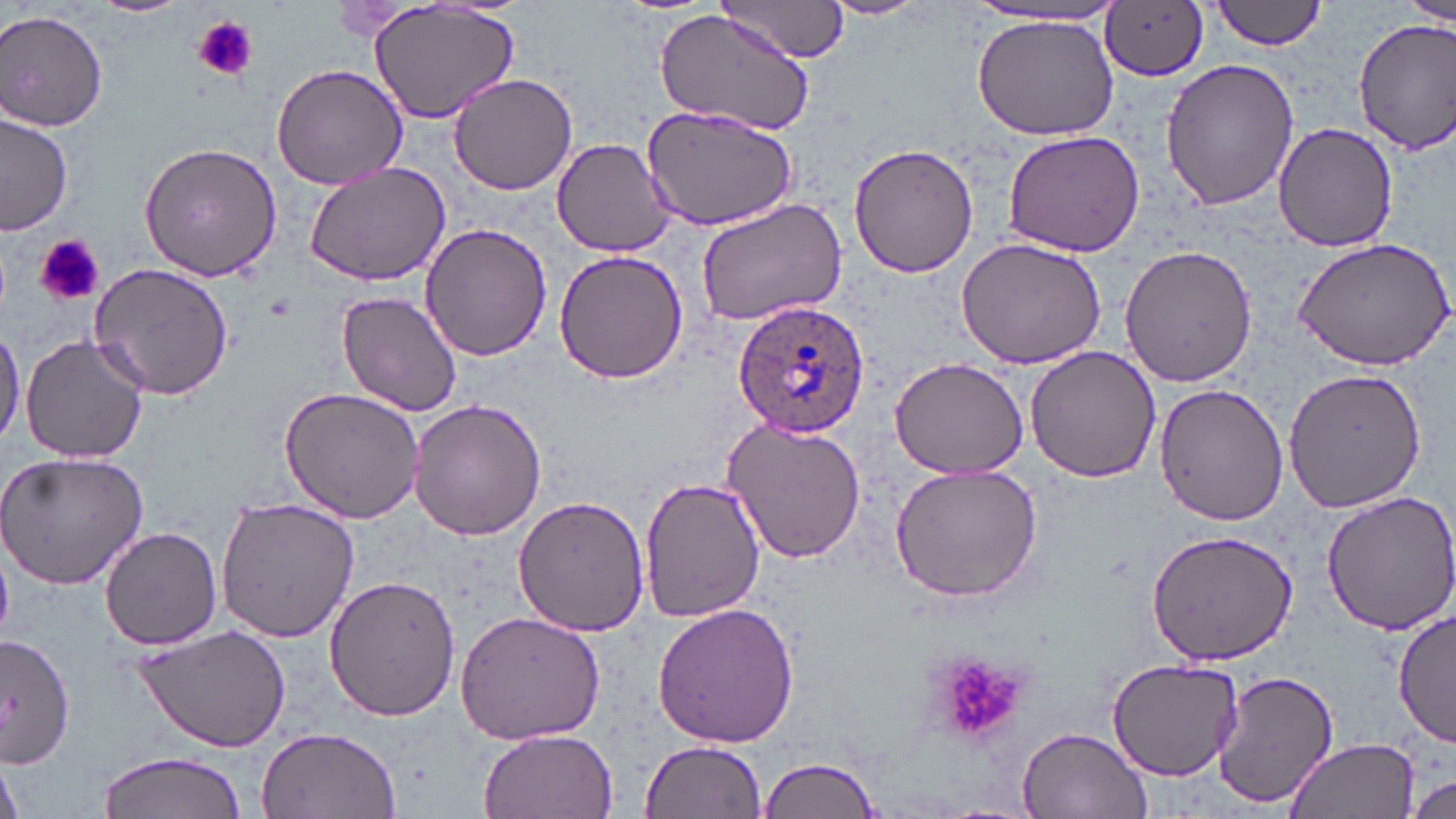

Approximate bounding boxes as [x1, y1, x2, y2] in pixels. Platelet locations: [193, 15, 257, 80], [36, 234, 103, 308], [925, 652, 1035, 746]. Uninfected red blood cell locations: [92, 0, 188, 17], [365, 0, 521, 127], [718, 0, 849, 62], [822, 0, 933, 20], [1208, 0, 1331, 51], [1392, 0, 1456, 33], [1101, 2, 1210, 82], [652, 3, 821, 141], [959, 5, 1129, 30], [0, 8, 110, 132], [970, 12, 1122, 141], [1354, 18, 1456, 153], [1159, 58, 1299, 208], [270, 62, 408, 190], [449, 73, 578, 195], [642, 106, 797, 231], [1, 114, 73, 236], [1272, 122, 1397, 253], [1002, 128, 1145, 256], [553, 138, 675, 256], [139, 141, 282, 283], [849, 142, 979, 278], [303, 161, 452, 286], [695, 198, 847, 327], [417, 221, 552, 363], [1292, 235, 1456, 370], [954, 237, 1107, 368], [1120, 244, 1257, 387], [555, 248, 687, 386], [88, 262, 234, 401], [338, 290, 462, 417], [0, 322, 24, 447], [18, 332, 149, 464], [1024, 348, 1162, 484], [889, 355, 1030, 479], [1282, 364, 1430, 514], [278, 385, 428, 525], [1153, 385, 1290, 527], [409, 398, 549, 541], [721, 416, 868, 566], [0, 450, 147, 589], [888, 462, 1043, 603], [636, 472, 767, 625], [1320, 490, 1456, 636], [215, 495, 360, 644], [514, 495, 651, 636], [99, 526, 223, 649], [1144, 530, 1299, 665], [324, 574, 460, 723], [651, 601, 800, 749], [1393, 607, 1456, 749], [454, 610, 606, 745], [130, 624, 292, 755], [0, 637, 74, 771], [1106, 659, 1246, 780], [1211, 669, 1341, 811], [1014, 724, 1152, 818], [257, 728, 402, 818], [480, 731, 618, 819], [1283, 736, 1421, 819], [641, 741, 766, 818], [96, 751, 248, 819], [756, 755, 885, 819], [0, 757, 26, 819], [1408, 773, 1455, 817]. Plasmodium ovale-infected red blood cell locations: [734, 298, 868, 438]. Slide-level diagnosis: Plasmodium ovale. May-Grünwald-Giemsa-stained preparation. Thin blood smear. One field of a larger specimen. Image is 1456×819 pixels. Captured at 1000x magnification. Optical microscopy.